Locate every uninfected red blood cell.
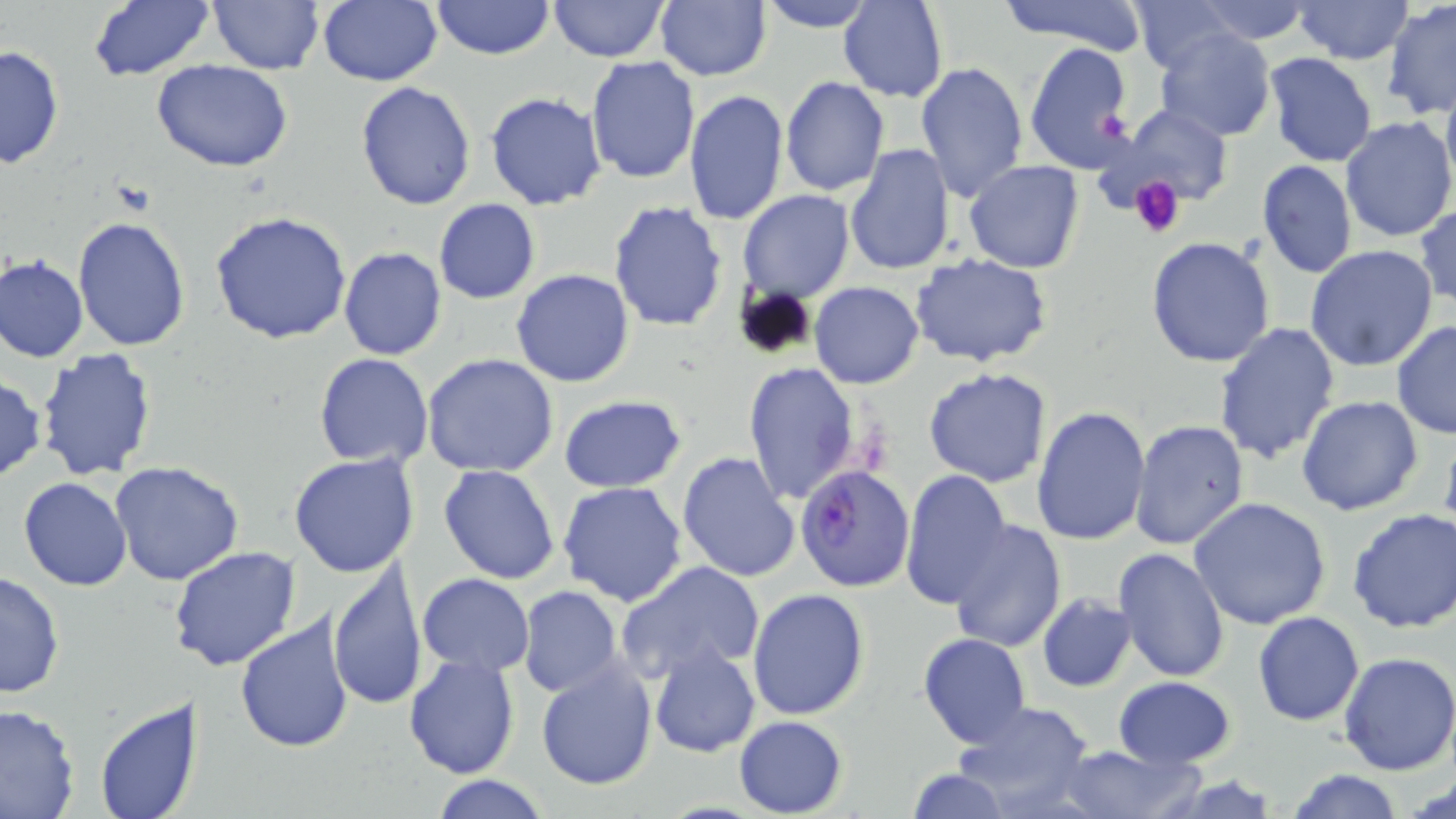

Approximate bounding boxes as (x1, y1, x2, y2) in pixels.
Uninfected red blood cells: (433, 0, 553, 59), (548, 0, 670, 63), (655, 0, 770, 81), (998, 0, 1149, 50), (1191, 0, 1316, 44), (1293, 0, 1412, 67), (208, 1, 323, 74), (316, 1, 443, 86), (758, 1, 873, 32), (1129, 1, 1242, 73), (1383, 1, 1456, 120), (87, 2, 214, 80), (838, 2, 948, 101), (1153, 28, 1278, 143), (1024, 40, 1135, 176), (0, 45, 64, 171), (1263, 52, 1378, 166), (585, 55, 702, 184), (151, 58, 294, 173), (913, 60, 1029, 203), (780, 77, 889, 197), (1441, 80, 1456, 197), (356, 81, 476, 212), (683, 90, 789, 226), (483, 91, 608, 211), (1115, 106, 1230, 207), (1340, 116, 1456, 244), (845, 145, 955, 275), (1256, 158, 1357, 278), (964, 160, 1084, 273), (738, 190, 854, 302), (434, 199, 540, 304), (607, 201, 729, 333), (1414, 203, 1456, 309), (208, 209, 354, 344), (73, 217, 192, 353), (1146, 237, 1276, 369), (1305, 246, 1441, 371), (338, 247, 447, 362), (1, 253, 88, 362), (911, 253, 1056, 369), (511, 268, 635, 387), (809, 281, 923, 389), (1211, 321, 1340, 467), (1391, 322, 1456, 441), (35, 347, 158, 482), (422, 352, 559, 478), (314, 353, 434, 469), (742, 362, 862, 508), (922, 367, 1052, 488), (0, 377, 47, 485), (558, 395, 688, 493), (1296, 395, 1423, 516), (1031, 405, 1151, 546), (1131, 420, 1250, 551), (676, 450, 802, 581), (289, 452, 419, 576), (109, 461, 244, 587), (439, 464, 560, 584), (899, 470, 1014, 610), (19, 477, 132, 590), (558, 482, 689, 607), (1190, 496, 1334, 630), (1347, 506, 1456, 634), (947, 521, 1067, 653), (173, 545, 302, 672), (1114, 548, 1230, 683), (615, 559, 765, 686), (329, 562, 429, 710), (0, 570, 65, 701), (417, 573, 535, 675), (518, 586, 623, 697), (747, 588, 871, 720), (1037, 593, 1136, 693), (1252, 611, 1365, 726), (234, 612, 356, 756), (918, 632, 1031, 748), (646, 643, 760, 758), (1337, 652, 1456, 776), (403, 653, 521, 777), (534, 661, 656, 790), (1114, 676, 1236, 768), (93, 697, 199, 818), (952, 700, 1097, 815), (0, 704, 78, 819), (734, 715, 847, 818), (1054, 745, 1193, 819), (905, 766, 1013, 819), (1287, 767, 1405, 819), (428, 775, 552, 818).

Summary:
  - Plasmodium falciparum-infected red blood cell locations: (795, 464, 916, 591)
  - Platelet locations: (1127, 175, 1185, 238)
  - Slide-level diagnosis: Plasmodium falciparum
  - Magnification: 1000x
  - Field of view: single
  - Modality: light microscopy
  - Preparation: thin blood smear
  - Image size: 1456×819 pixels
  - Stain: May-Grünwald-Giemsa